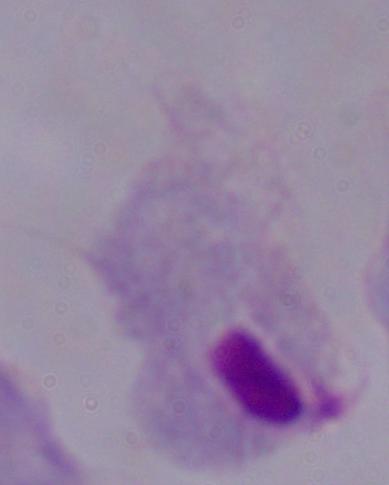
modality = micrograph
magnification = 1000x
identification = trichomonad